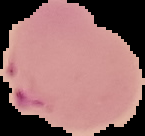
Image is 145×136 pixels. From a thin blood film. Malaria status: parasitized. Cell region segmented out of the field of view; the surrounding area is masked to black.